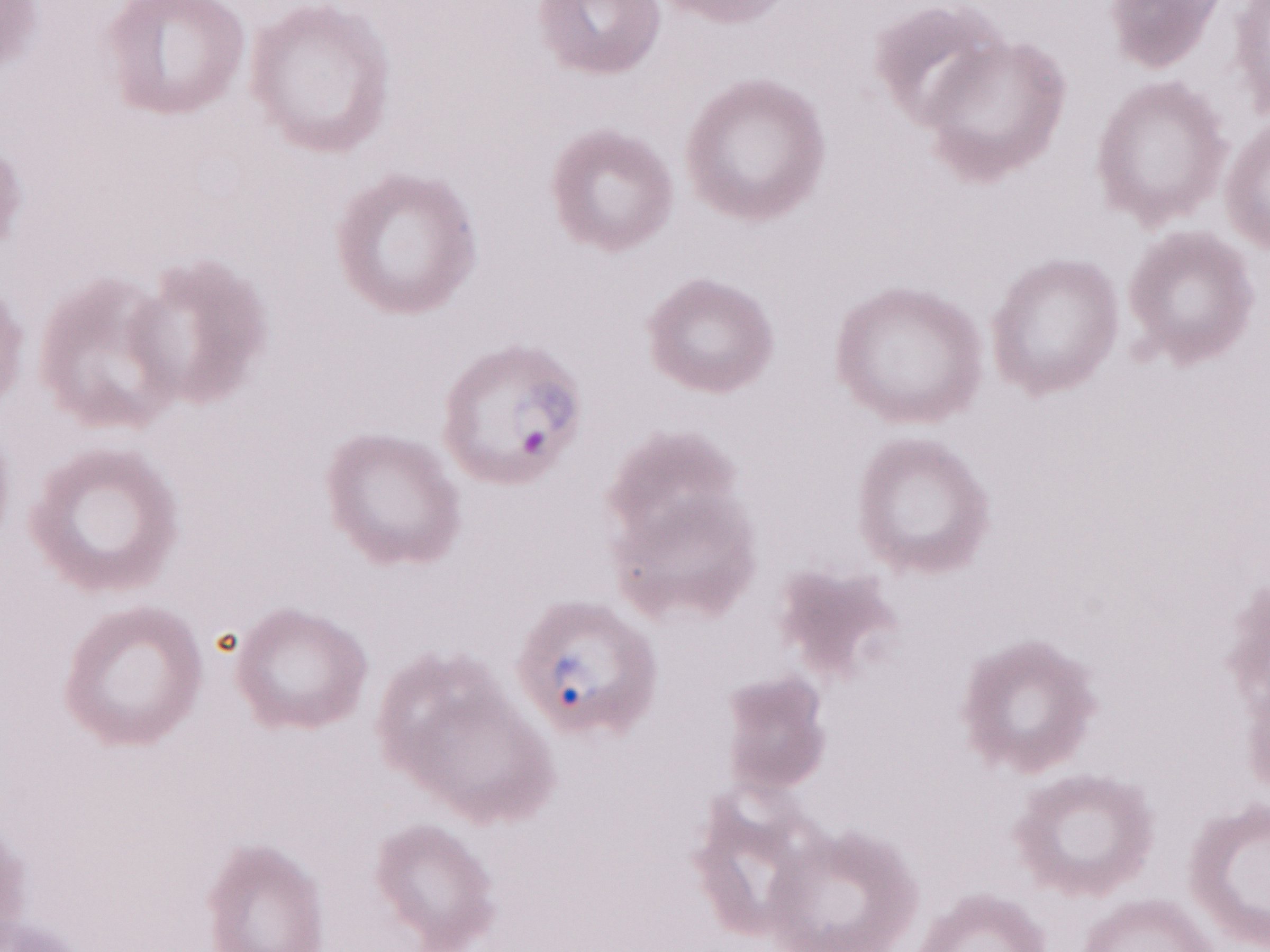
Olympus BX43 microscope, Olympus DP73 camera. One field of this slide. Image is 1270×952 pixels. Malaria diagnosis (patient-level): positive. May-Grünwald-Giemsa-stained preparation. Thin peripheral-blood smear. 1,000x magnification.